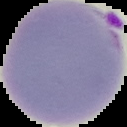
{
  "preparation": "thin blood film",
  "image_size": "127×127 pixels",
  "image_type": "cell region segmented out of the field of view; surrounding area masked to black",
  "malaria_status": "parasitized"
}